Point out each malaria parasite.
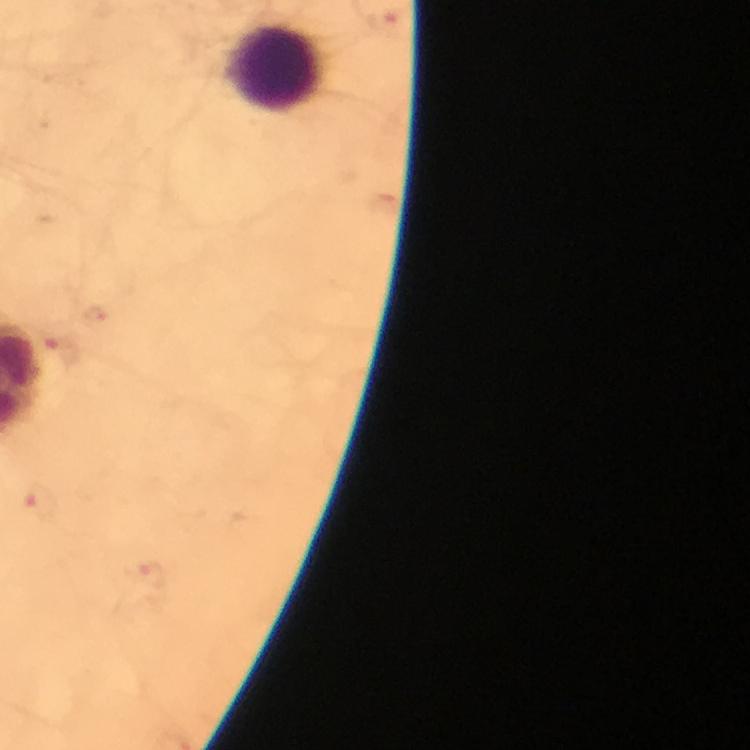
Approximate centers as (x, y) in pixels.
Malaria parasites: (384, 20), (65, 348), (41, 501), (148, 573).

context: from a malaria diagnostic workup
preparation: thick smear
magnification: 100x
image_size: 750×750 pixels
capture: smartphone camera through the microscope
immersion_oil: used
cropped_from: a single field of view
stain: Giemsa